Assess this cell for malaria.
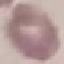

Uninfected.

Thin smear of blood. Giemsa-stained preparation. Automatically extracted cell patch, resized to 64 × 64 pixels. Acquired by smartphone through the microscope eyepiece.